Report the malaria status of this cell.
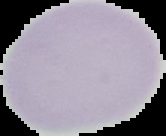
It is uninfected.

Image is 166×136 pixels. Segmented cell region on a black background. From a thin blood smear.